Point out each malaria parasite.
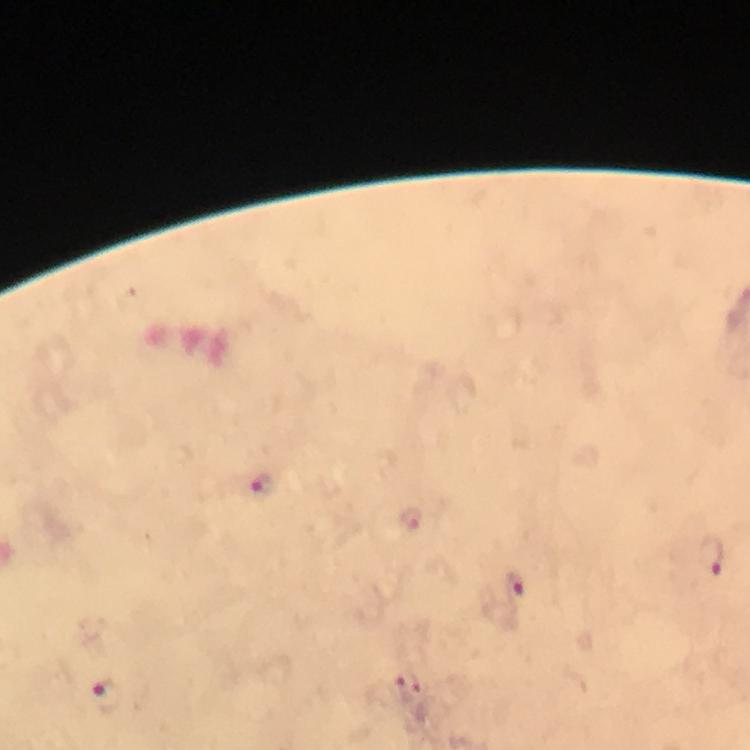
Approximate centers as [x, y] in pixels.
Malaria parasites: [261, 485], [410, 519], [712, 553], [514, 586], [410, 688], [107, 697].

image size = 750×750 pixels
magnification = 100x
context = from a diagnostic examination for malaria
stain = Giemsa
immersion oil = used
capture = smartphone photograph through a microscope
cropped from = a single field of view
preparation = thick blood film